Assess the morphology of the red blood cells.
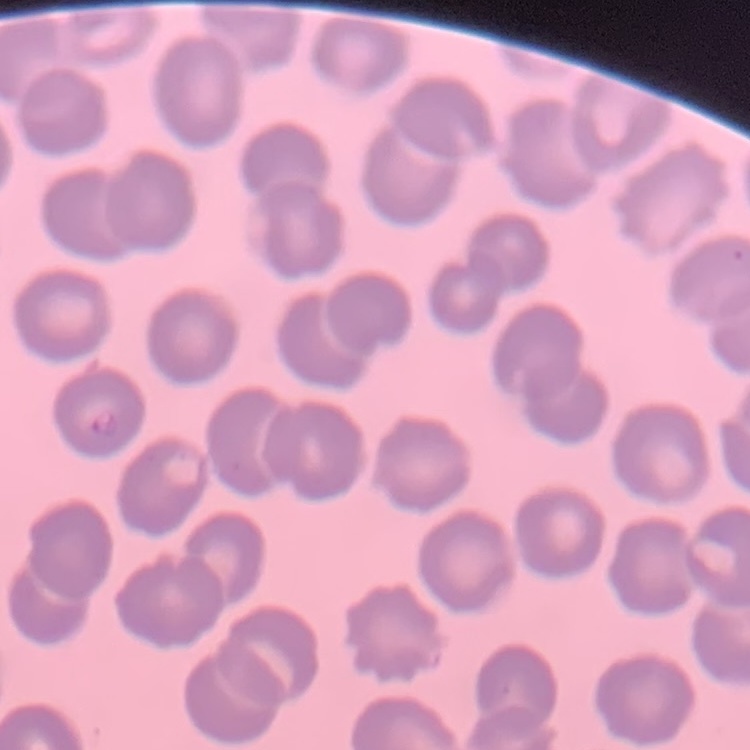
No rouleaux formation.

Field's or Giemsa stain. One tile cut from a larger photomicrograph. Thin blood film.